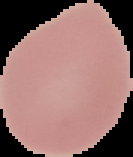

Summary:
  - Image type: cell region segmented out of the field of view; surrounding area masked to black
  - Malaria status: uninfected
  - Preparation: thin blood film
  - Image size: 133×157 pixels